Evaluate for malaria.
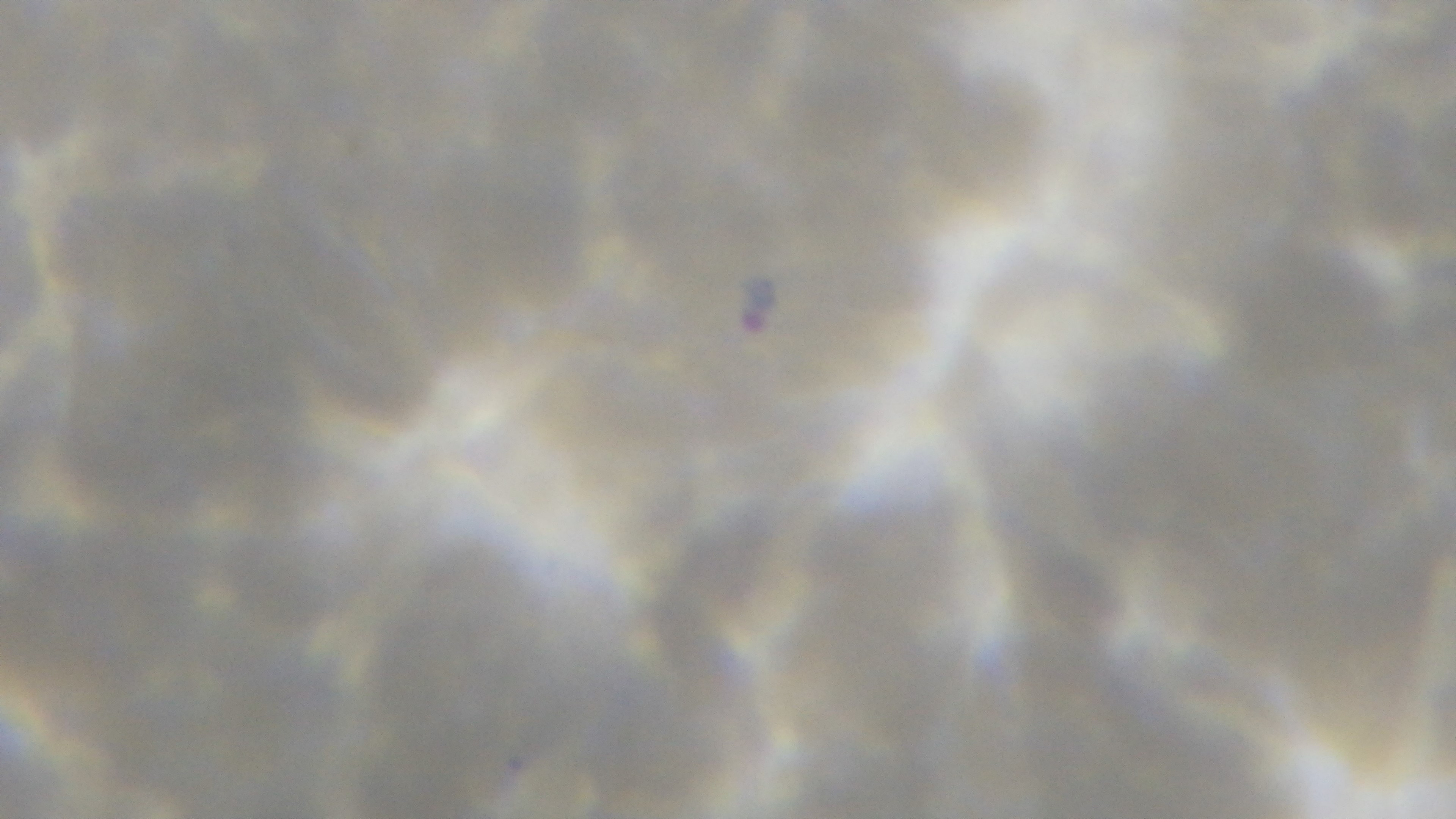
Infected.

preparation = thin blood film
modality = light microscopy
capture = mounted 4K digital camera
stain = Giemsa
objective = 100x oil immersion
field of view = one from the slide